Assess this cell for malaria.
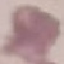

Uninfected.

preparation = thin blood smear
image type = cell patch, automatically extracted from a larger field of view and resized to 64 × 64 pixels
stain = Giemsa
capture = smartphone camera at the microscope eyepiece